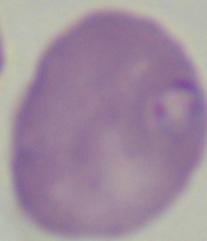

{
  "identification": "Babesia",
  "magnification": "1000x",
  "modality": "photomicrograph"
}